Name the parasite shown.
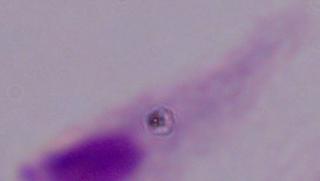

This is a trichomonad.

Micrograph. 1000x magnification.